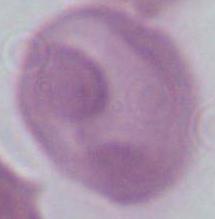
A red blood cell is shown. Micrograph. Captured at 1000x magnification.